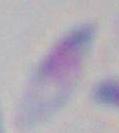 Captured at 1000x magnification. Toxoplasma gondii is shown. Photomicrograph.